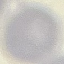

malaria status = uninfected
capture = smartphone camera at the microscope eyepiece
image type = cell patch, automatically extracted from a larger field of view and resized to 64 × 64 pixels
stain = Giemsa
preparation = thin smear